State which parasite is depicted.
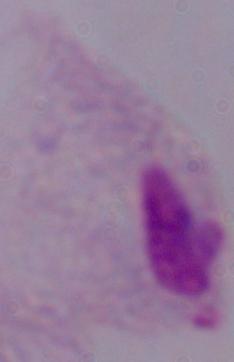

A trichomonad.

1000x magnification. Photomicrograph.